Outline each uninfected red blood cell.
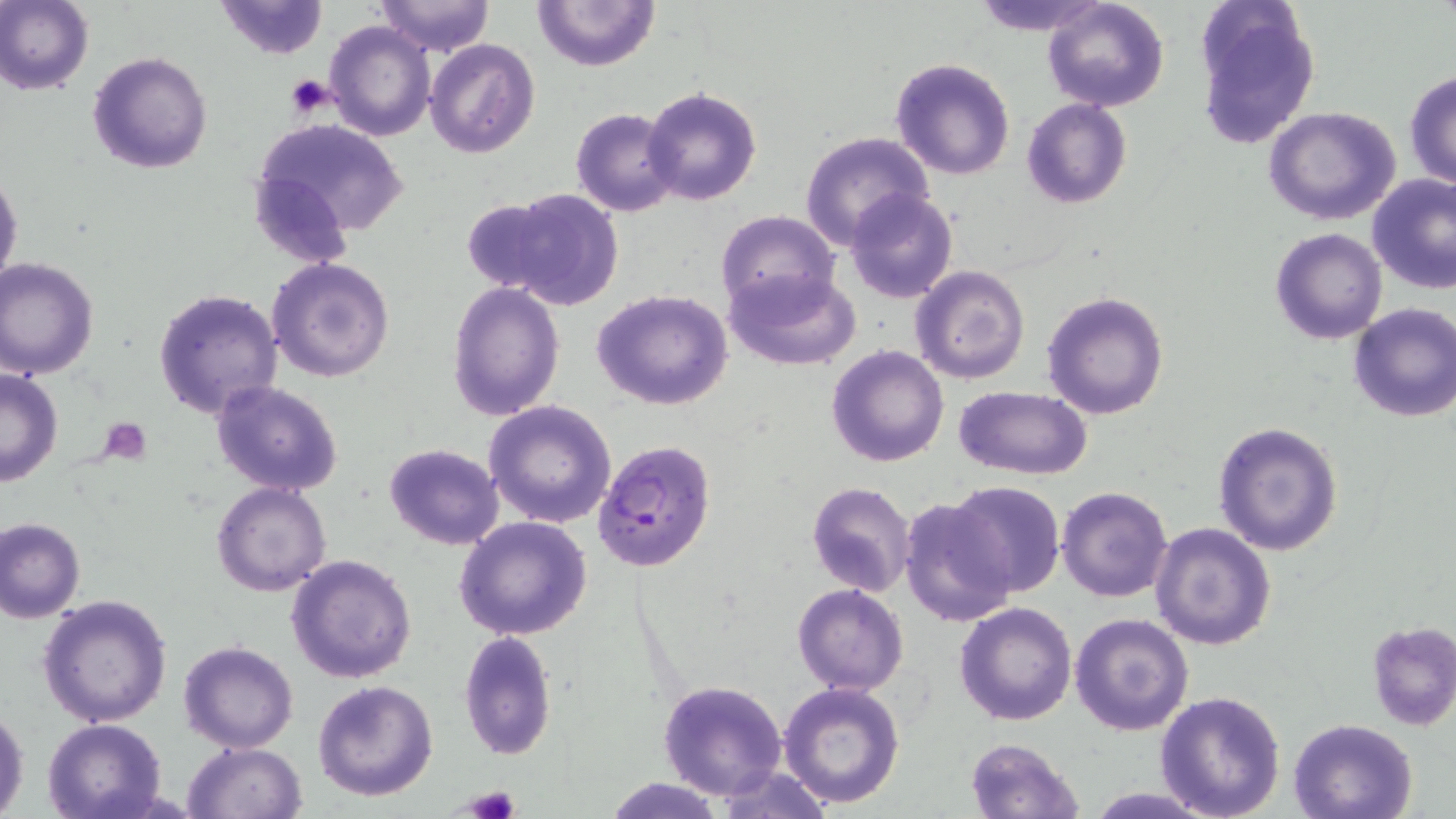
Approximate bounding boxes as (x1, y1, x2, y2) in pixels.
Uninfected red blood cells: (0, 0, 93, 95), (215, 0, 327, 60), (533, 0, 658, 71), (969, 0, 1113, 36), (1042, 0, 1168, 112), (1194, 0, 1322, 149), (375, 1, 494, 56), (324, 21, 435, 140), (425, 37, 540, 157), (87, 50, 213, 175), (890, 58, 1017, 181), (1405, 69, 1456, 188), (644, 87, 760, 205), (1022, 97, 1132, 208), (572, 106, 683, 216), (1264, 107, 1403, 224), (255, 117, 409, 240), (799, 133, 935, 251), (0, 170, 23, 291), (1367, 174, 1456, 294), (488, 187, 625, 311), (845, 188, 959, 305), (716, 210, 839, 315), (1269, 228, 1388, 345), (267, 257, 394, 383), (0, 258, 100, 381), (724, 265, 863, 370), (911, 265, 1030, 383), (447, 281, 566, 419), (152, 287, 284, 420), (592, 289, 735, 410), (1041, 289, 1170, 421), (1347, 302, 1456, 423), (825, 344, 949, 467), (0, 366, 63, 486), (210, 380, 345, 496), (953, 384, 1092, 480), (484, 399, 617, 529), (1213, 421, 1345, 557), (383, 443, 506, 550), (807, 481, 917, 597), (949, 481, 1064, 598), (212, 482, 332, 596), (1057, 486, 1173, 602), (899, 496, 1017, 628), (0, 516, 86, 623), (454, 516, 593, 641), (1148, 522, 1277, 650), (286, 555, 419, 683), (792, 583, 908, 695), (37, 594, 172, 727), (954, 601, 1078, 726), (1069, 613, 1195, 735), (1365, 621, 1456, 730), (457, 629, 558, 762), (178, 640, 301, 753), (657, 679, 788, 801), (312, 680, 439, 802), (779, 682, 906, 808), (1155, 690, 1286, 819), (1, 704, 30, 816), (42, 718, 166, 819), (1288, 718, 1420, 819), (963, 737, 1085, 819), (184, 742, 307, 819), (710, 763, 837, 818), (605, 776, 726, 817), (1081, 787, 1223, 818).

Plasmodium falciparum-infected red blood cell locations: (593, 439, 716, 574). Platelet locations: (283, 74, 337, 118), (100, 417, 151, 461), (457, 786, 521, 819). Slide-level diagnosis: Plasmodium falciparum. Captured at 1000x magnification. Image is 1456×819 pixels. Optical microscopy. Thin blood film. Single field of view. May-Grünwald-Giemsa-stained preparation.